Locate every Plasmodium falciparum-infected red blood cell.
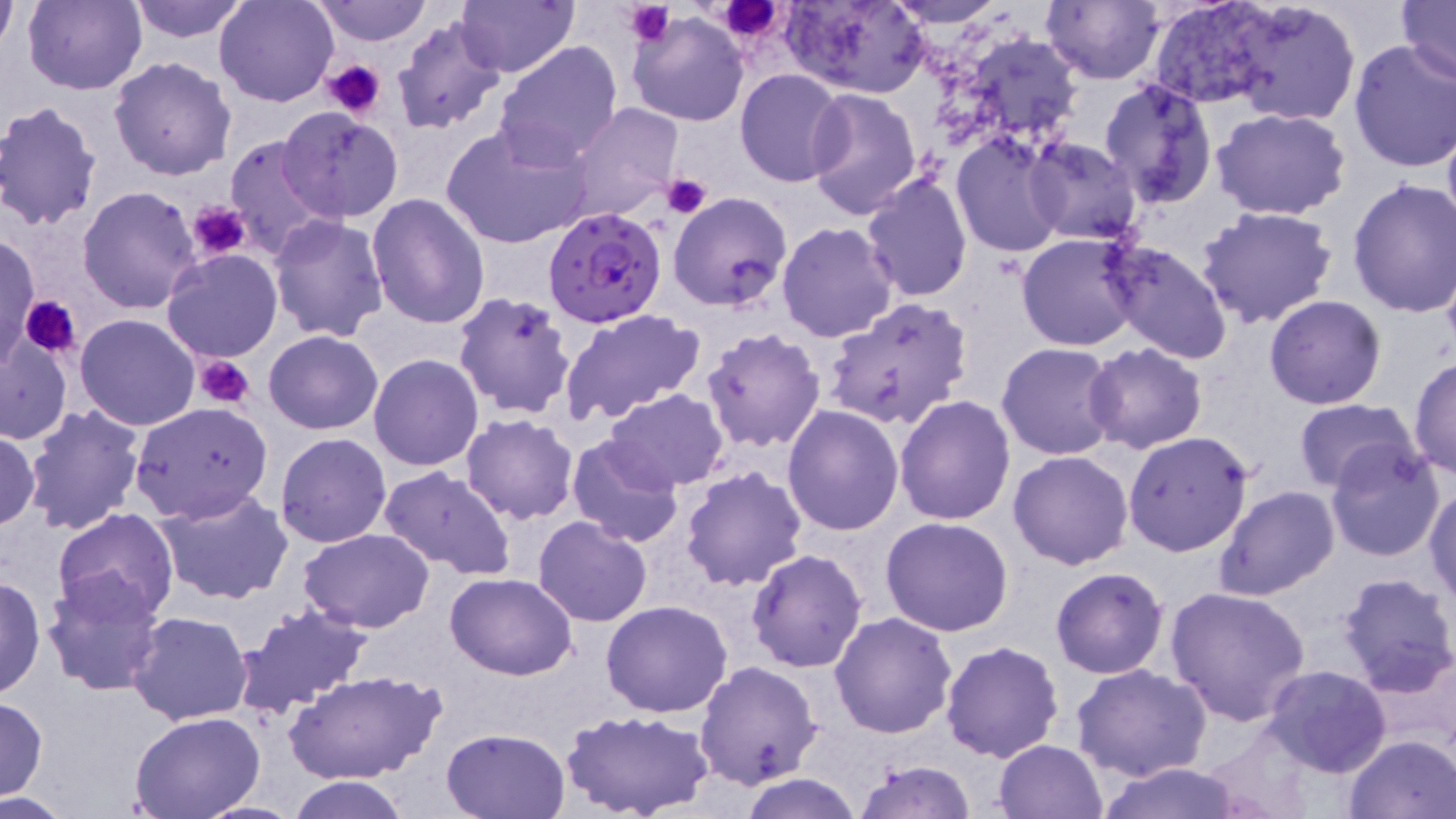

Approximate bounding boxes as (x1, y1, x2, y2) in pixels.
Plasmodium falciparum-infected red blood cells: (544, 206, 668, 328).

Uninfected red blood cell locations: (22, 0, 146, 95), (125, 0, 254, 45), (215, 0, 340, 107), (314, 0, 434, 47), (454, 0, 579, 77), (782, 0, 930, 97), (885, 0, 1011, 27), (1042, 0, 1164, 85), (1397, 0, 1455, 87), (1223, 1, 1362, 128), (1149, 2, 1282, 107), (0, 5, 18, 52), (626, 11, 748, 127), (391, 16, 507, 134), (925, 25, 1086, 163), (1347, 39, 1456, 175), (494, 41, 622, 167), (109, 56, 237, 180), (735, 69, 852, 186), (1098, 79, 1219, 209), (804, 87, 923, 219), (0, 101, 103, 231), (566, 102, 682, 222), (278, 108, 403, 223), (1211, 108, 1352, 220), (1441, 109, 1456, 246), (441, 121, 592, 251), (951, 134, 1067, 259), (224, 135, 334, 258), (1023, 137, 1143, 245), (860, 173, 972, 303), (1346, 177, 1456, 318), (77, 187, 203, 315), (669, 191, 794, 312), (367, 192, 491, 329), (1194, 205, 1339, 332), (268, 215, 390, 342), (776, 222, 899, 342), (1016, 232, 1144, 351), (2, 233, 41, 364), (1099, 239, 1235, 365), (161, 249, 283, 363), (452, 292, 578, 421), (1264, 295, 1386, 409), (823, 296, 974, 432), (559, 307, 706, 425), (74, 313, 201, 431), (701, 327, 826, 451), (263, 330, 383, 434), (0, 334, 74, 445), (997, 343, 1120, 461), (1083, 343, 1208, 455), (369, 354, 484, 472), (1410, 355, 1455, 481), (605, 389, 728, 492), (895, 395, 1015, 524), (1292, 399, 1422, 495), (129, 401, 274, 523), (782, 405, 905, 535), (21, 406, 146, 537), (461, 414, 579, 524), (0, 428, 41, 533), (1123, 430, 1255, 558), (275, 432, 391, 548), (566, 435, 686, 549), (1324, 442, 1446, 561), (1009, 451, 1133, 570), (679, 465, 807, 591), (377, 466, 518, 582), (1425, 484, 1456, 605), (1216, 486, 1341, 600), (155, 488, 296, 606), (52, 508, 180, 625), (533, 515, 652, 626), (881, 517, 1015, 637), (299, 527, 437, 633), (746, 549, 867, 674), (1050, 566, 1169, 679), (40, 570, 167, 696), (445, 572, 578, 680), (1335, 572, 1456, 694), (1, 573, 46, 703), (1167, 586, 1312, 725), (601, 600, 732, 717), (235, 604, 371, 717), (127, 611, 254, 726), (830, 611, 959, 738), (939, 640, 1064, 762), (695, 661, 822, 789), (1071, 664, 1212, 783), (1263, 664, 1391, 777), (286, 669, 444, 786), (0, 698, 49, 798), (562, 710, 712, 819), (131, 713, 264, 819), (441, 726, 571, 817), (1342, 734, 1456, 818), (993, 739, 1109, 819), (852, 759, 978, 819), (1091, 762, 1252, 818), (736, 774, 867, 818), (283, 775, 413, 818), (0, 792, 72, 817). Platelet locations: (624, 0, 676, 47), (712, 0, 784, 41), (325, 59, 384, 117), (663, 172, 712, 218), (191, 200, 249, 261), (18, 295, 81, 357), (193, 353, 257, 409). Slide-level diagnosis: Plasmodium falciparum. Thin blood smear. 1000x magnification. May-Grünwald-Giemsa-stained preparation. One field of a larger specimen. Light microscopy. Image is 1456×819 pixels.